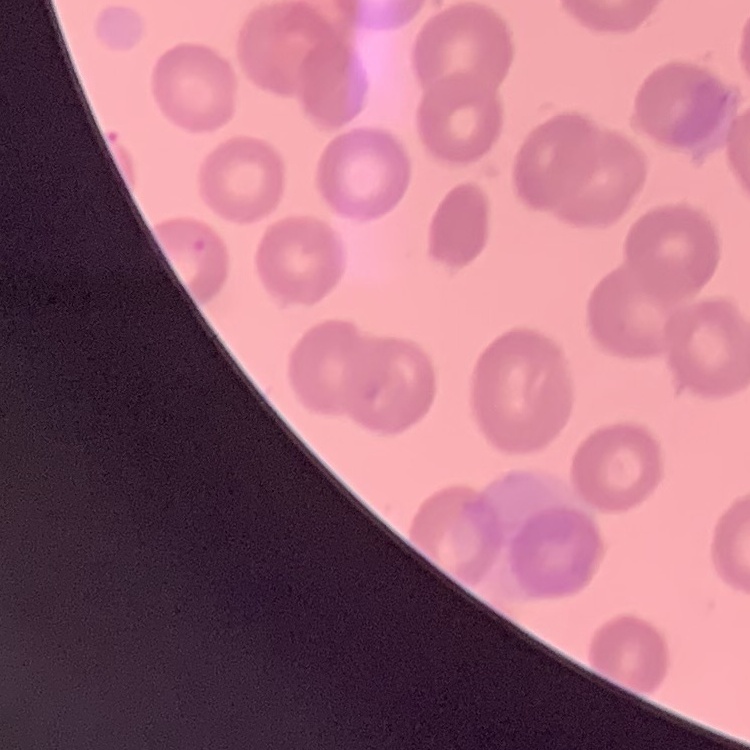

Summary:
  - Red blood cell morphology: no rouleaux formation
  - Image type: one tile cut from a larger photomicrograph
  - Stain: Field's or Giemsa
  - Preparation: thin blood film